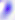
Summary:
  - Identification: Toxoplasma gondii
  - Modality: photomicrograph
  - Magnification: 400x